Assess this cell for malaria.
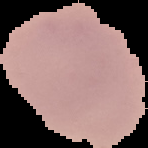
Uninfected.

Summary:
  - Preparation: thin blood smear
  - Image size: 148×148 pixels
  - Image type: segmented cell region on a black background